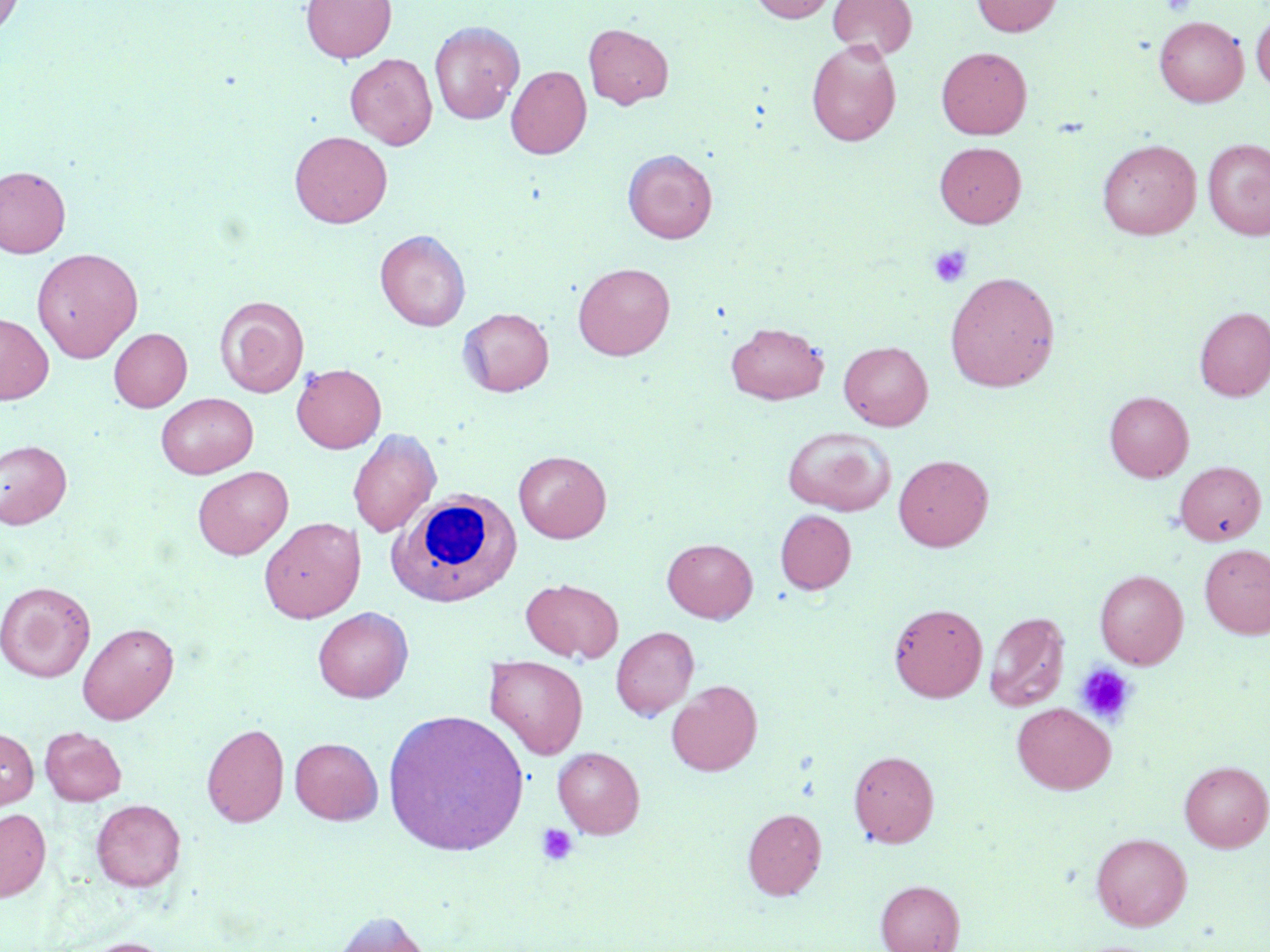
Summary:
  - Coordinate format: approximate bounding boxes as (x1, y1, x2, y2) in pixels
  - White blood cell locations: (389, 489, 522, 607)
  - Uninfected red blood cell locations: (0, 0, 25, 38), (301, 0, 396, 63), (750, 0, 836, 23), (828, 0, 917, 60), (972, 0, 1062, 36), (1251, 11, 1270, 92), (1154, 15, 1248, 107), (430, 21, 524, 124), (583, 23, 674, 109), (806, 39, 902, 146), (936, 46, 1032, 139), (345, 53, 437, 149), (506, 65, 591, 159), (289, 130, 392, 228), (1203, 138, 1270, 240), (1097, 139, 1201, 240), (934, 142, 1026, 228), (623, 148, 717, 243), (0, 165, 71, 258), (375, 230, 471, 331), (32, 247, 144, 362), (573, 262, 675, 360), (944, 271, 1060, 392), (214, 295, 309, 398), (1195, 307, 1270, 401), (458, 308, 554, 397), (0, 313, 53, 404), (726, 321, 829, 405), (109, 328, 192, 411), (838, 340, 933, 430), (292, 363, 386, 453), (1104, 391, 1193, 482), (156, 393, 258, 478), (782, 426, 896, 516), (347, 428, 440, 538), (0, 439, 72, 529), (514, 450, 611, 543), (894, 454, 993, 551), (1174, 461, 1266, 546), (192, 466, 293, 559), (774, 510, 856, 594), (259, 517, 365, 623), (663, 538, 757, 622), (1199, 543, 1270, 639), (1095, 570, 1188, 668), (520, 578, 623, 663), (0, 581, 95, 682), (889, 603, 987, 702), (312, 607, 413, 703), (984, 611, 1069, 712), (77, 622, 178, 724), (611, 626, 699, 720), (485, 657, 589, 759), (666, 680, 762, 776), (1012, 702, 1116, 795), (382, 709, 529, 857), (201, 723, 289, 827), (40, 727, 127, 805), (0, 728, 38, 810), (290, 737, 383, 824), (553, 746, 645, 839), (848, 750, 939, 847), (1180, 760, 1270, 852), (91, 799, 186, 892), (0, 808, 51, 901), (742, 808, 826, 900), (1090, 832, 1192, 930), (875, 880, 964, 952), (326, 910, 434, 952), (74, 937, 178, 952)
  - Platelet locations: (1162, 0, 1195, 17), (929, 245, 972, 288), (1075, 663, 1137, 725), (535, 822, 579, 866)
  - Slide-level diagnosis: negative for blood parasites
  - Stain: May-Grünwald-Giemsa
  - Image size: 1270×952 pixels
  - Field of view: single
  - Magnification: 1000x
  - Preparation: thin blood film
  - Modality: light microscopy